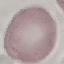

Result: no malaria parasites detected. Thin smear of blood. Automatically extracted cell patch, resized to 64 × 64 pixels. Giemsa-stained preparation. Photographed with a smartphone camera at the microscope eyepiece.